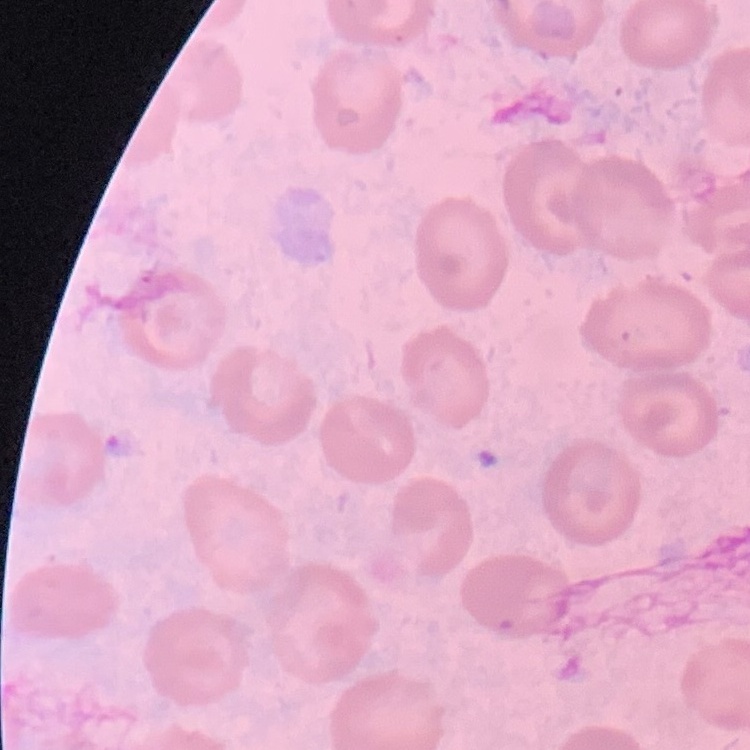
The red blood cells show no rouleaux formation. Field's or Giemsa stain. Thin blood smear. One tile cut from a larger photomicrograph.